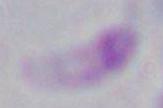
Captured at 1000x magnification. Toxoplasma gondii is shown. Micrograph.